Give the position of every leukocyte visible.
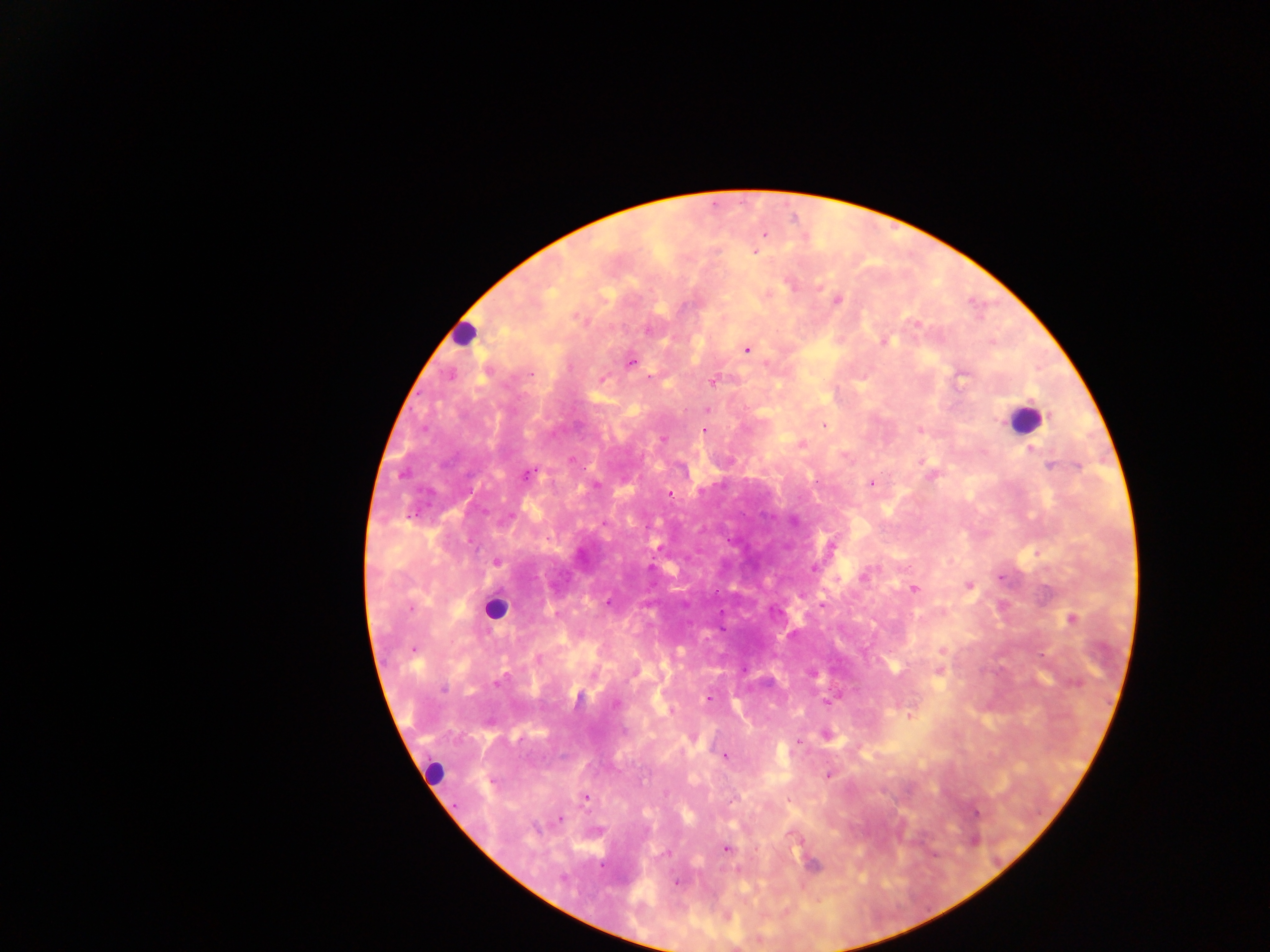
Approximate centers as {x, y} in pixels.
Leukocytes: {466, 335}, {1025, 419}, {497, 610}, {439, 772}.

Summary:
  - Malaria parasite locations: {766, 235}, {755, 251}, {838, 297}, {914, 321}, {647, 328}, {883, 341}, {746, 351}, {630, 362}, {769, 364}, {964, 374}, {532, 375}, {603, 376}, {961, 380}, {712, 383}, {707, 409}, {823, 424}, {920, 430}, {703, 433}, {661, 439}, {801, 445}, {1031, 449}, {920, 459}, {1050, 465}, {585, 467}, {525, 475}, {932, 476}, {869, 483}, {470, 491}, {671, 495}, {416, 514}, {408, 517}, {793, 520}, {647, 527}, {547, 538}, {727, 539}, {830, 546}, {653, 558}, {496, 562}, {813, 567}, {865, 576}, {1003, 578}, {967, 585}, {913, 588}, {717, 590}, {608, 602}, {721, 610}, {774, 612}, {1070, 618}, {721, 629}, {895, 666}, {810, 674}, {1047, 676}, {498, 681}, {444, 690}, {709, 697}, {577, 699}, {829, 699}, {615, 705}, {909, 716}, {798, 741}, {725, 757}, {829, 774}, {644, 781}, {584, 797}, {557, 821}, {726, 848}, {678, 882}
  - Image size: 1270×952 pixels
  - Preparation: thick blood smear
  - Field of view: single
  - Country: Ghana
  - Capture: mobile-phone photograph through a microscope